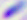
{
  "modality": "micrograph",
  "identification": "Toxoplasma gondii",
  "magnification": "400x"
}